Assess the morphology of the red blood cells.
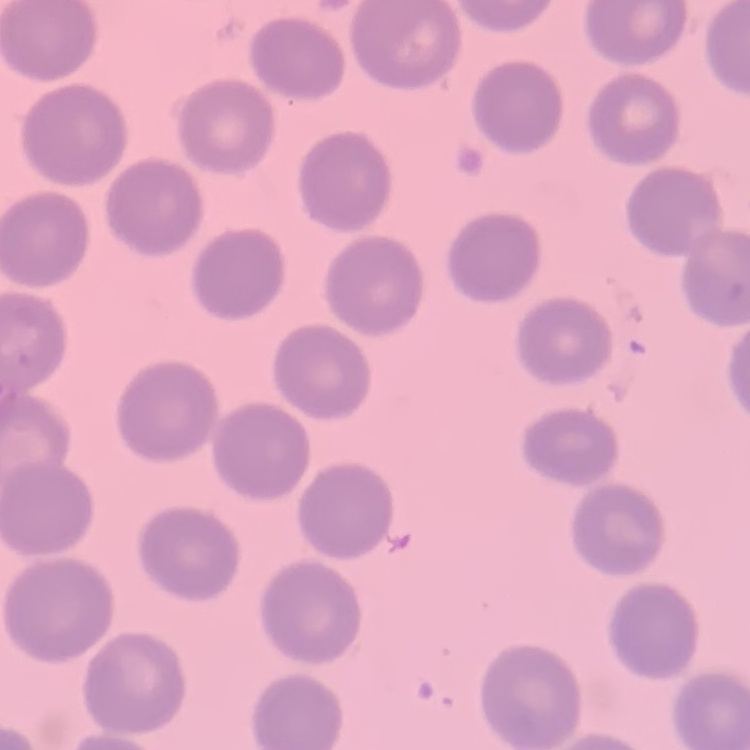
They show no rouleaux formation.

image type = one tile cut from a larger photomicrograph
preparation = thin blood smear
stain = Field's or Giemsa